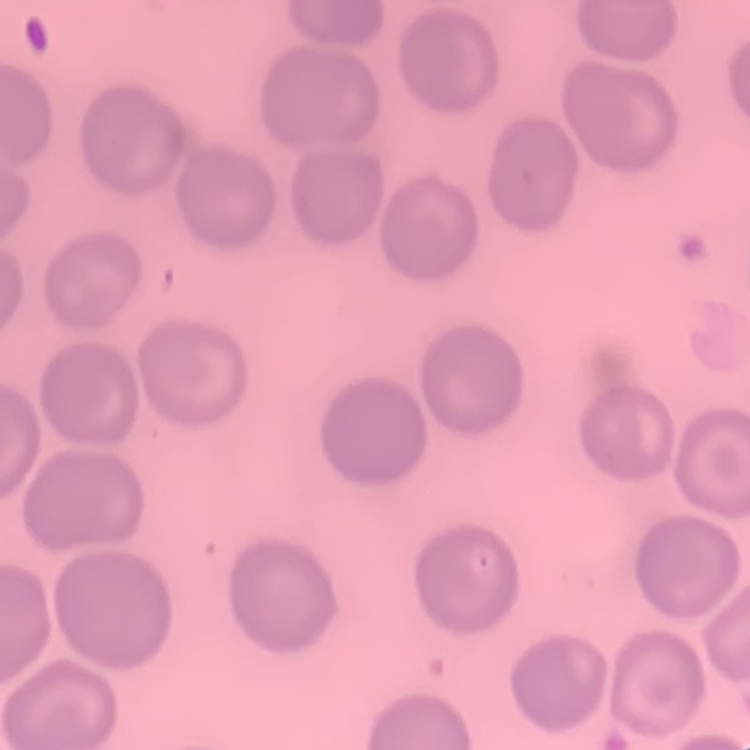
Summary:
  - Red blood cell morphology: no rouleaux formation
  - Stain: Field's or Giemsa
  - Image type: square crop of a larger photomicrograph
  - Preparation: thin peripheral smear